Describe the morphology of the red blood cells.
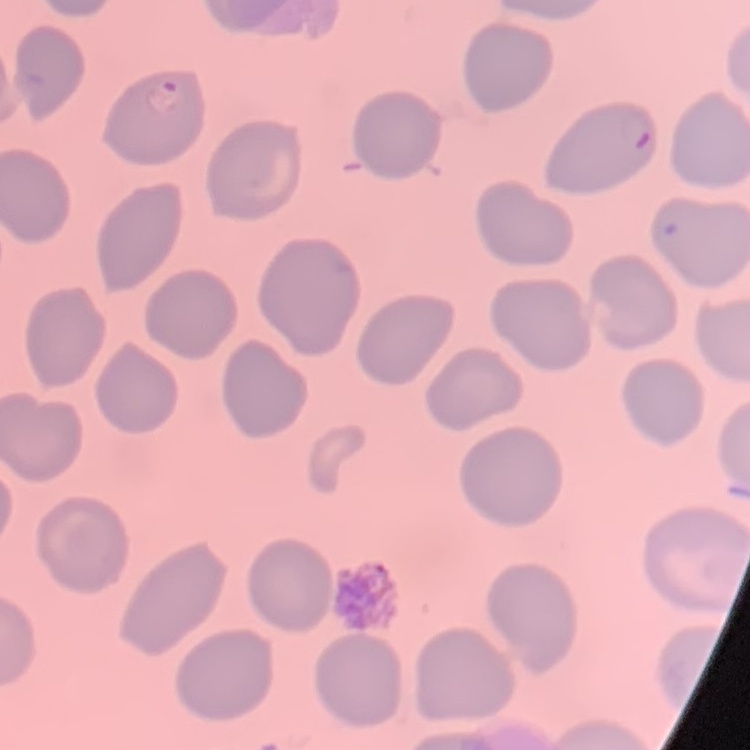
No rouleaux formation.

image type = one tile cut from a larger photomicrograph
stain = Field's or Giemsa
preparation = thin peripheral smear